Classify this cell by malaria status.
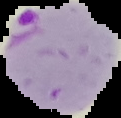
Parasitized.

{
  "preparation": "thin blood film",
  "image_size": "121×118 pixels",
  "image_type": "cell region segmented out of the field of view; surrounding area masked to black"
}